Give the extent of all Plasmodium parasites.
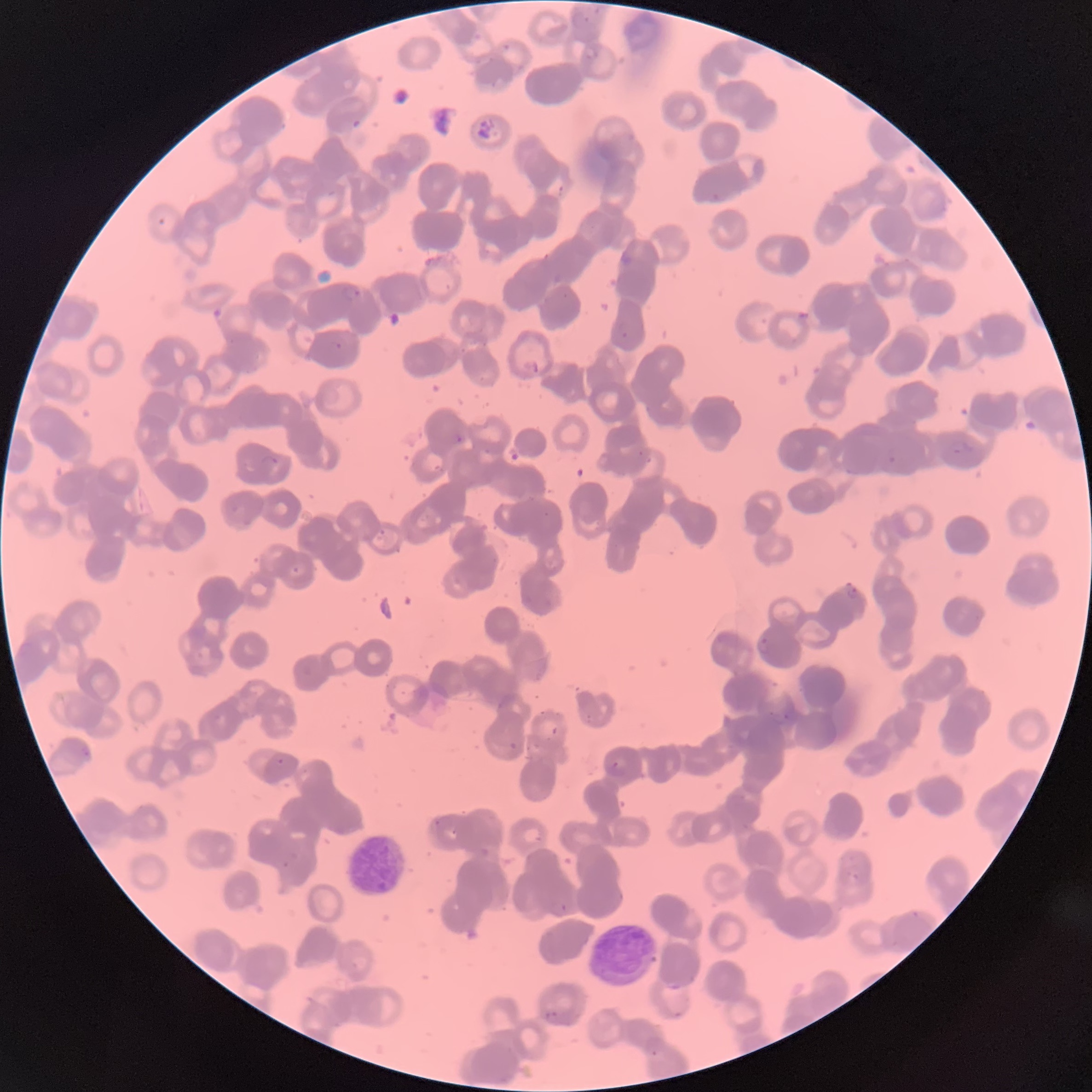

Approximate bounding boxes as named x1/y1/x2/y2 corners in pixels.
Plasmodium parasites: (x1=557, y1=183, x2=567, y2=195), (x1=342, y1=283, x2=362, y2=302), (x1=618, y1=323, x2=630, y2=340), (x1=330, y1=340, x2=342, y2=352), (x1=452, y1=431, x2=464, y2=444), (x1=637, y1=450, x2=645, y2=457), (x1=886, y1=451, x2=899, y2=465), (x1=260, y1=455, x2=279, y2=466), (x1=645, y1=456, x2=653, y2=464), (x1=377, y1=529, x2=387, y2=541), (x1=292, y1=566, x2=300, y2=574), (x1=846, y1=585, x2=859, y2=599), (x1=757, y1=636, x2=772, y2=656), (x1=782, y1=707, x2=793, y2=724), (x1=508, y1=741, x2=518, y2=750), (x1=80, y1=744, x2=93, y2=761), (x1=276, y1=758, x2=285, y2=766), (x1=608, y1=761, x2=626, y2=777), (x1=545, y1=1010, x2=558, y2=1024).

Summary:
  - White blood cell locations: (x1=343, y1=832, x2=410, y2=898), (x1=590, y1=919, x2=659, y2=991)
  - Red blood cell morphology: rouleaux formation
  - Image size: 1092×1092 pixels
  - Modality: optical microscopy
  - Preparation: thin blood smear